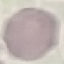

Summary:
  - Result: no malaria parasites seen
  - Capture: smartphone through the microscope eyepiece
  - Image type: cell patch, automatically extracted from a larger field of view and resized to 64 × 64 pixels
  - Stain: Giemsa
  - Preparation: thin smear